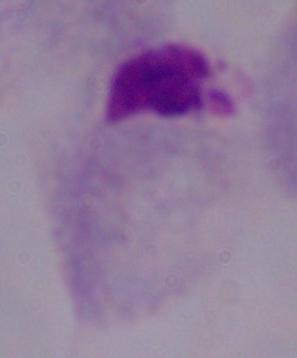

Summary:
  - Modality: micrograph
  - Magnification: 1000x
  - Identification: trichomonad